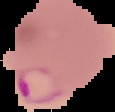

Image is 115×112 pixels. Cell region segmented out of the field of view; the surrounding area is masked to black. From a thin blood smear. Malaria status: parasitized.